State the preparation type.
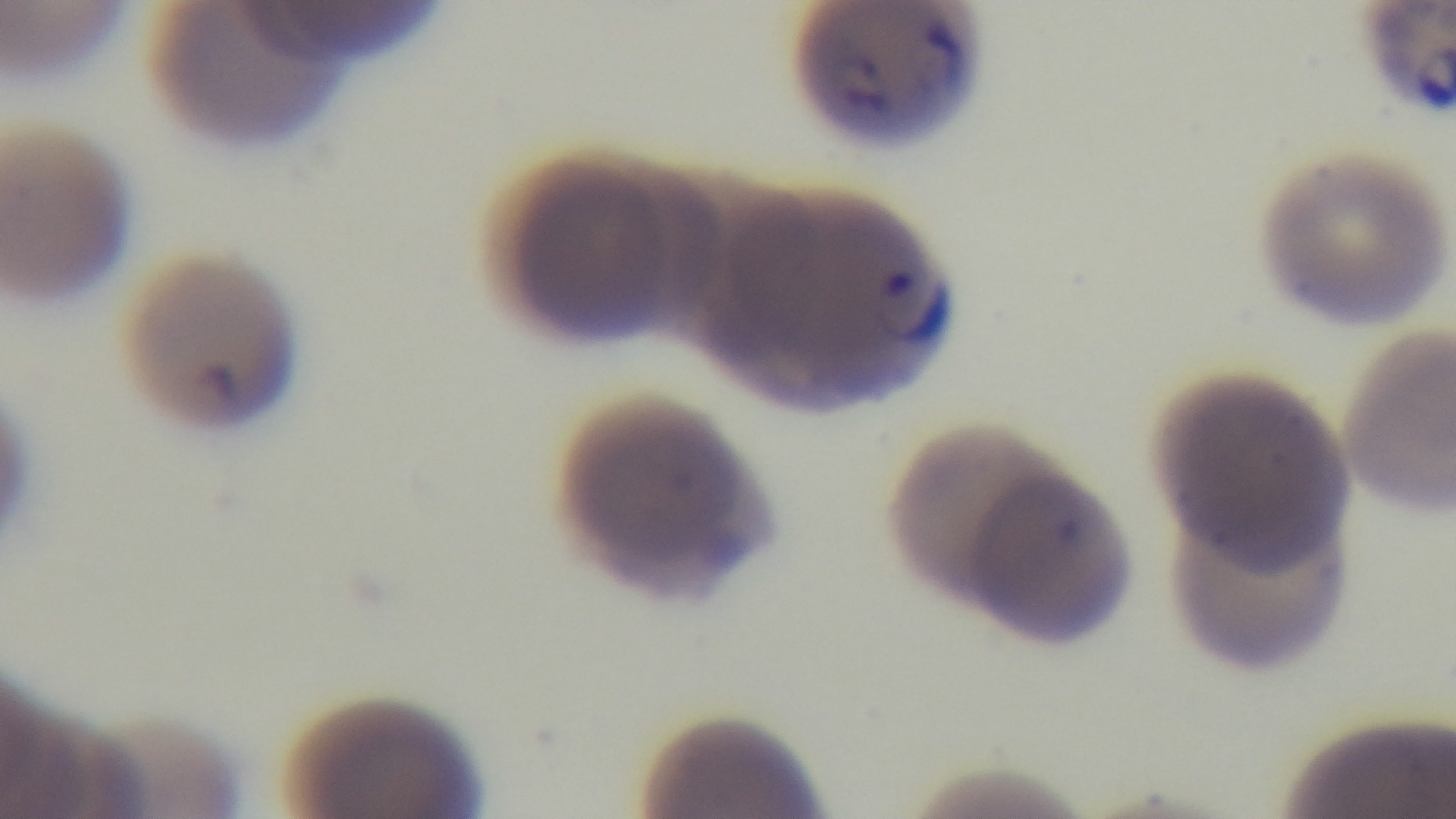
A thin smear.

{
  "malaria_status": "infected",
  "capture": "mounted 4K digital camera",
  "objective": "100x oil immersion",
  "field_of_view": "single",
  "stain": "Giemsa",
  "modality": "light microscopy"
}